Outline each blood parasite and name the species.
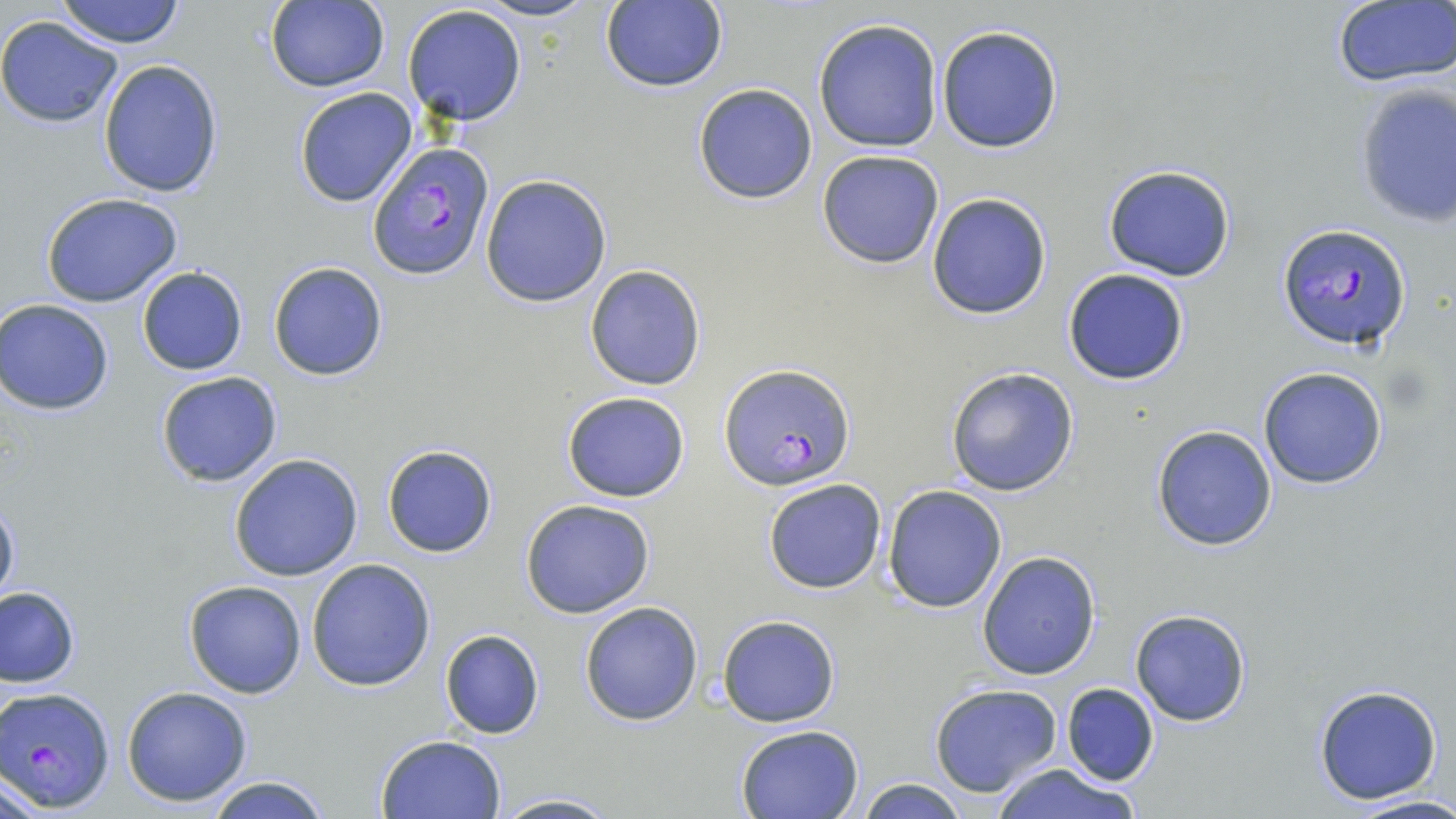
Approximate bounding boxes as named x1/y1/x2/y2 corners in pixels.
Plasmodium falciparum-infected red blood cells: (x1=368, y1=144, x2=494, y2=280), (x1=1276, y1=222, x2=1412, y2=351), (x1=721, y1=363, x2=854, y2=491), (x1=2, y1=687, x2=115, y2=809).
No Plasmodium ovale, Plasmodium malariae, Plasmodium vivax, Babesia divergens, or Trypanosoma brucei observed.

Summary:
  - Uninfected red blood cell locations: (x1=54, y1=0, x2=187, y2=48), (x1=471, y1=0, x2=602, y2=23), (x1=1332, y1=0, x2=1456, y2=88), (x1=598, y1=1, x2=727, y2=93), (x1=262, y1=2, x2=390, y2=91), (x1=402, y1=5, x2=528, y2=127), (x1=0, y1=16, x2=124, y2=129), (x1=813, y1=18, x2=945, y2=153), (x1=935, y1=24, x2=1065, y2=153), (x1=98, y1=59, x2=223, y2=197), (x1=1352, y1=82, x2=1456, y2=229), (x1=692, y1=83, x2=819, y2=204), (x1=293, y1=87, x2=417, y2=207), (x1=816, y1=150, x2=945, y2=269), (x1=1101, y1=165, x2=1238, y2=282), (x1=480, y1=173, x2=612, y2=306), (x1=40, y1=192, x2=183, y2=307), (x1=926, y1=193, x2=1052, y2=319), (x1=267, y1=261, x2=388, y2=382), (x1=584, y1=265, x2=706, y2=391), (x1=136, y1=266, x2=248, y2=375), (x1=1062, y1=268, x2=1191, y2=386), (x1=0, y1=298, x2=115, y2=416), (x1=1258, y1=367, x2=1388, y2=489), (x1=946, y1=368, x2=1080, y2=496), (x1=155, y1=370, x2=282, y2=488), (x1=562, y1=390, x2=690, y2=502), (x1=1151, y1=424, x2=1279, y2=552), (x1=381, y1=444, x2=497, y2=558), (x1=229, y1=453, x2=364, y2=582), (x1=763, y1=478, x2=887, y2=594), (x1=881, y1=484, x2=1007, y2=612), (x1=0, y1=494, x2=20, y2=614), (x1=520, y1=498, x2=655, y2=619), (x1=976, y1=551, x2=1102, y2=681), (x1=306, y1=557, x2=437, y2=690), (x1=183, y1=580, x2=308, y2=699), (x1=1, y1=585, x2=80, y2=688), (x1=579, y1=602, x2=704, y2=726), (x1=1130, y1=608, x2=1251, y2=726), (x1=718, y1=614, x2=839, y2=727), (x1=440, y1=629, x2=544, y2=739), (x1=929, y1=682, x2=1062, y2=796), (x1=1059, y1=683, x2=1160, y2=786), (x1=1313, y1=683, x2=1445, y2=805), (x1=120, y1=685, x2=253, y2=807), (x1=734, y1=724, x2=864, y2=819), (x1=375, y1=733, x2=507, y2=819), (x1=992, y1=763, x2=1142, y2=819), (x1=3, y1=772, x2=53, y2=819), (x1=205, y1=775, x2=332, y2=819), (x1=853, y1=778, x2=971, y2=818), (x1=489, y1=792, x2=621, y2=819), (x1=1347, y1=794, x2=1456, y2=819)
  - Slide-level diagnosis: Plasmodium falciparum
  - Field of view: one of a larger specimen
  - Stain: May-Grünwald-Giemsa
  - Modality: optical microscopy
  - Preparation: thin blood smear
  - Magnification: 1000x
  - Image size: 1456×819 pixels